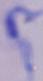
Photomicrograph. A trypanosome is shown. Captured at 1000x magnification.